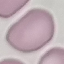

malaria status = uninfected
image type = cell patch, automatically extracted from a larger field of view and resized to 64 × 64 pixels
preparation = thin blood film
stain = Giemsa
capture = smartphone through the microscope eyepiece